Locate every Trypanosoma brucei.
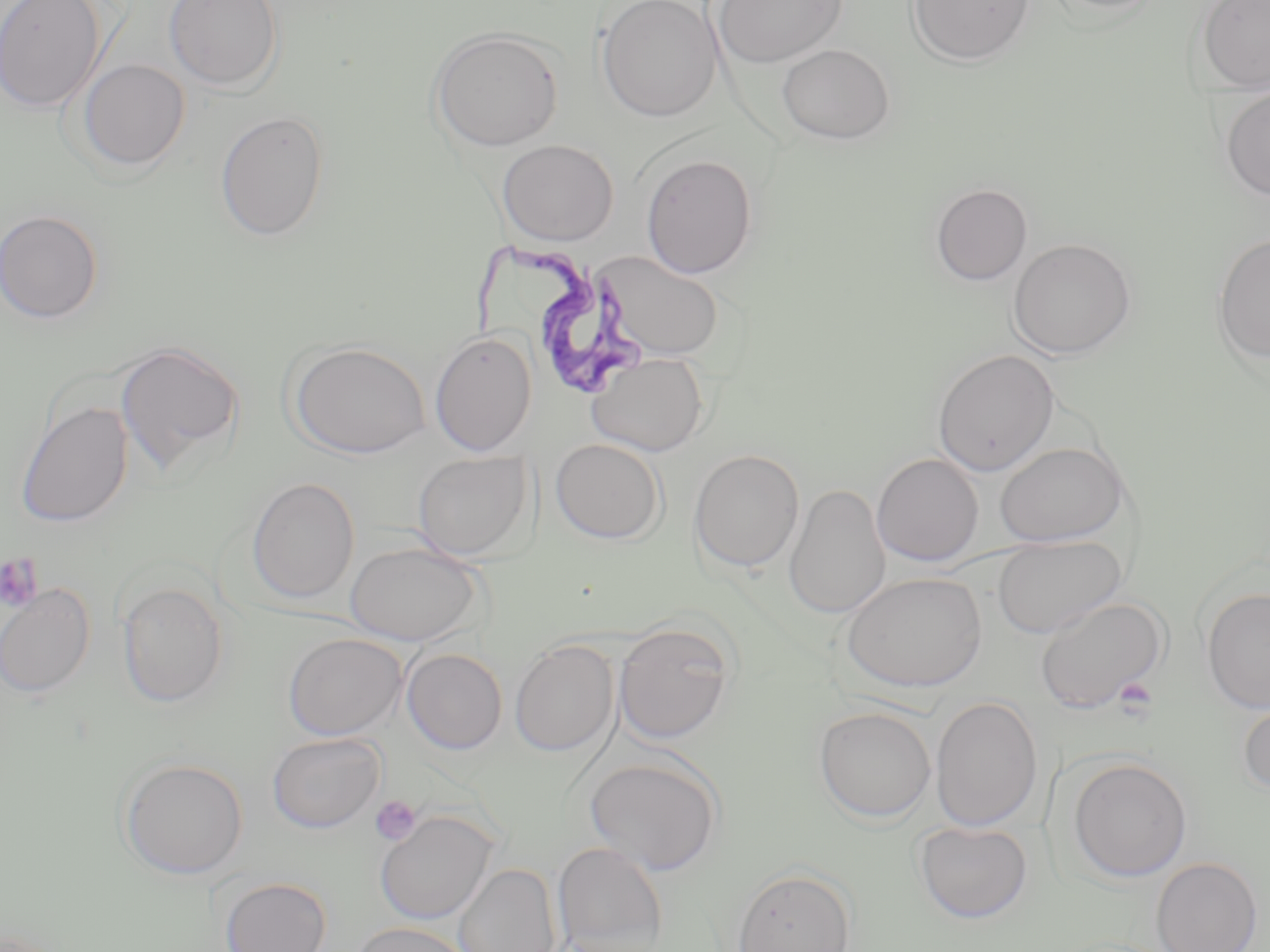
Approximate bounding boxes as (x1,y1)-(x2,y2) corner pairs in pixels.
Trypanosoma brucei: (473,244)-(645,396).

Summary:
  - Platelet locations: (0,554)-(44,612), (1113,678)-(1159,721), (370,795)-(422,846)
  - Uninfected red blood cell locations: (0,0)-(106,114), (163,0)-(284,92), (596,0)-(723,121), (712,0)-(849,68), (906,0)-(1036,66), (1042,0)-(1167,17), (1195,0)-(1270,91), (428,27)-(564,152), (777,43)-(895,145), (76,58)-(190,172), (1219,90)-(1270,201), (215,110)-(330,241), (496,139)-(619,246), (640,153)-(758,279), (930,183)-(1033,286), (0,208)-(104,325), (1212,233)-(1270,365), (1007,237)-(1137,359), (596,250)-(724,361), (429,330)-(538,457), (114,340)-(245,478), (288,341)-(430,459), (932,349)-(1059,476), (587,351)-(709,456), (15,400)-(133,528), (550,438)-(666,544), (994,442)-(1128,547), (689,449)-(805,573), (412,451)-(533,561), (872,453)-(984,566), (245,476)-(360,605), (783,483)-(890,620), (992,534)-(1127,639), (344,541)-(483,646), (841,571)-(987,692), (116,580)-(230,709), (0,583)-(95,698), (1201,586)-(1270,714), (1033,595)-(1168,714), (613,622)-(735,744), (283,632)-(407,740), (510,639)-(619,757), (401,648)-(508,754), (930,695)-(1043,832), (1237,699)-(1270,796), (813,706)-(937,822), (267,732)-(386,833), (584,755)-(723,875), (1067,757)-(1192,882), (119,758)-(248,879), (375,809)-(498,925), (914,820)-(1033,924), (552,842)-(669,952), (1151,857)-(1263,952), (453,862)-(560,952), (732,867)-(856,952), (219,876)-(332,952), (352,922)-(474,952)
  - Slide-level diagnosis: Trypanosoma brucei
  - Magnification: 1000x
  - Modality: optical microscopy
  - Preparation: thin blood smear
  - Field of view: one of a larger specimen
  - Stain: May-Grünwald-Giemsa
  - Image size: 1270×952 pixels